Identify the cell.
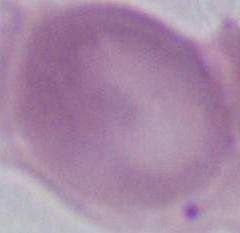

An erythrocyte.

Summary:
  - Modality: photomicrograph
  - Magnification: 1000x